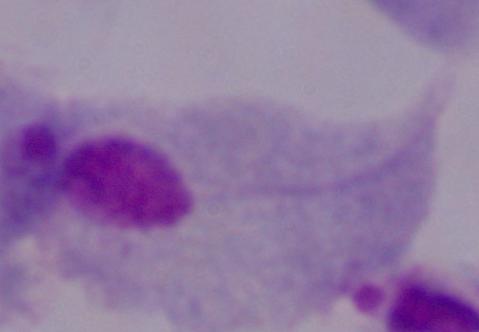

1000x magnification. Photomicrograph. A trichomonad is seen.